Report the malaria status of this cell.
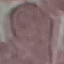

It is uninfected.

stain: Giemsa
image_type: automatically extracted cell patch, resized to 64 × 64 pixels
capture: smartphone camera at the microscope eyepiece
preparation: thin blood film